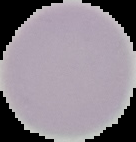

Summary:
  - Image type: segmented cell region with the area outside set to black
  - Preparation: thin blood smear
  - Image size: 136×142 pixels
  - Result: no Plasmodium parasites seen